Give the position of every Plasmodium parasite.
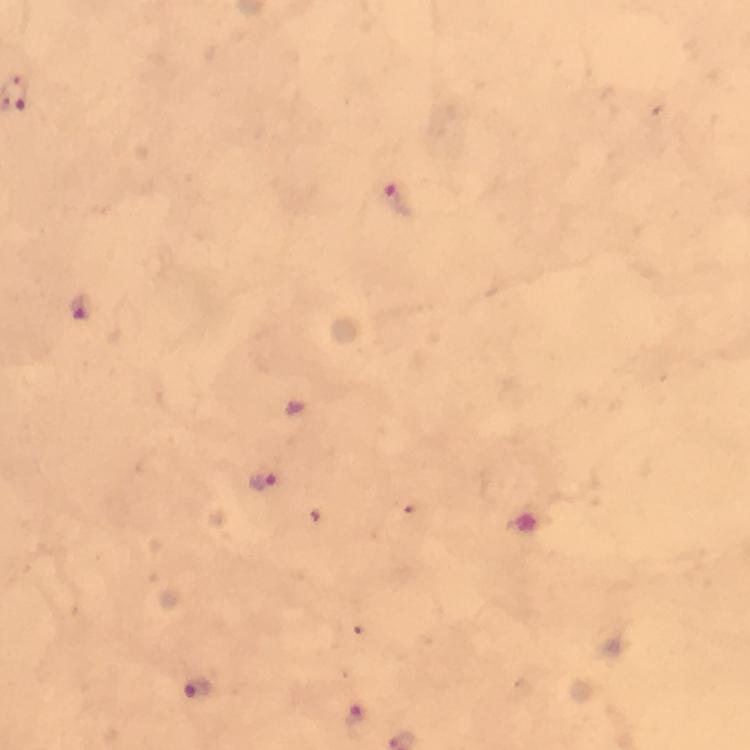
Approximate centers as [x, y] in pixels.
Plasmodium parasites: [400, 203], [78, 308], [263, 483], [197, 689], [358, 721].

Thick blood smear. Photographed through the microscope with a smartphone camera. Image is 750×750 pixels. Giemsa-stained preparation. A crop from one field of view. At 100x magnification. Immersion oil applied. From a diagnostic examination for malaria.